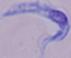

Summary:
  - Identification: trypanosome
  - Modality: photomicrograph
  - Magnification: 1000x